Identify the preparation type.
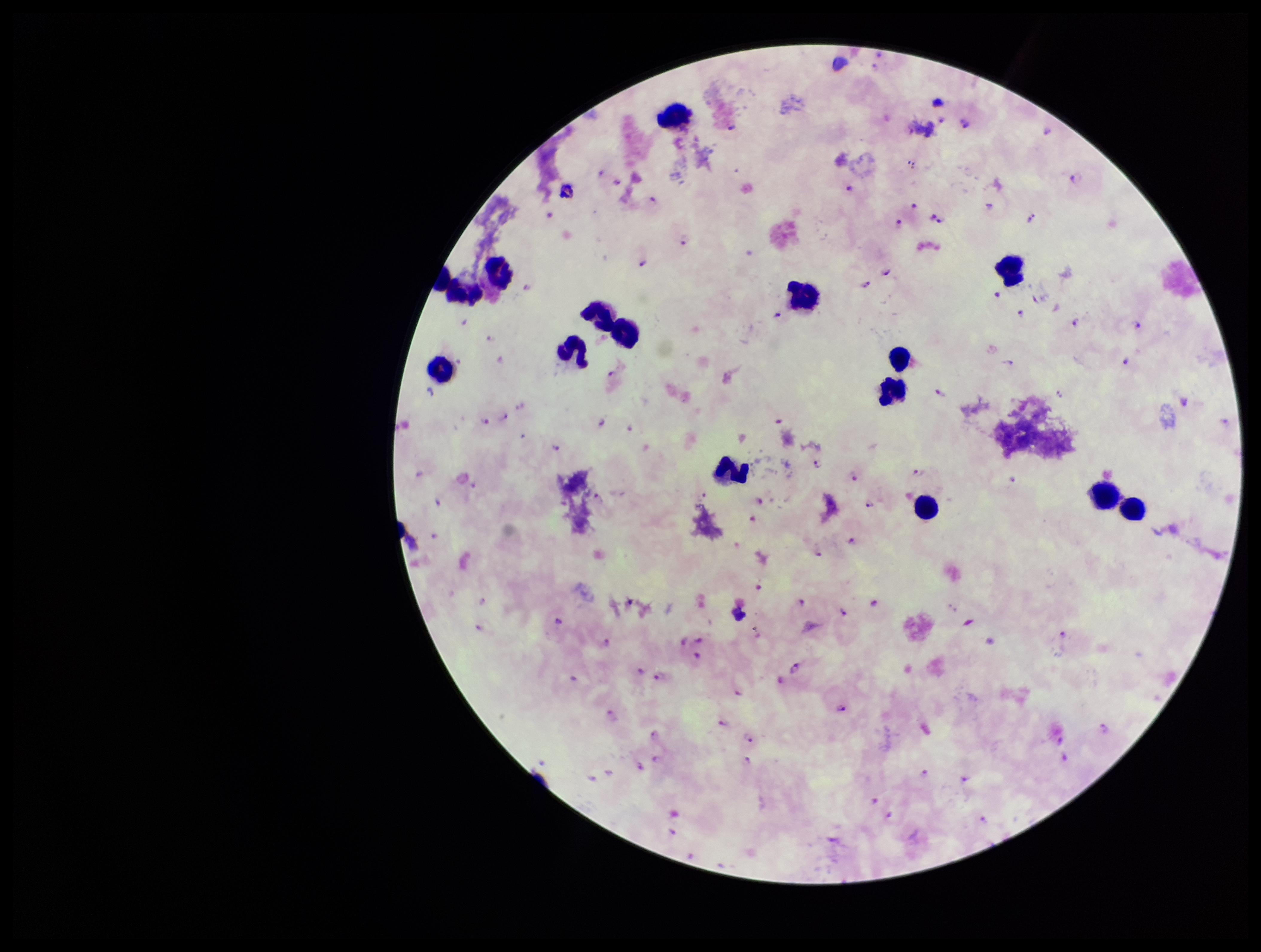

It is a thick blood smear.

Summary:
  - Species reported for this patient: Plasmodium falciparum
  - Plasmodium parasites: seen
  - Patient malaria status: infected
  - Capture: smartphone photograph through the microscope eyepiece
  - Stain: Giemsa
  - Image size: 1261×952 pixels
  - Leukocyte count: 14
  - Field of view: one from this slide
  - Parasite count: 99